Draw a bounding box around every parasitised red blood cell, every trophozoite, every gametocyte, every leukocyte, and every artifact (platelet-like body, stain precipitate, or debris).
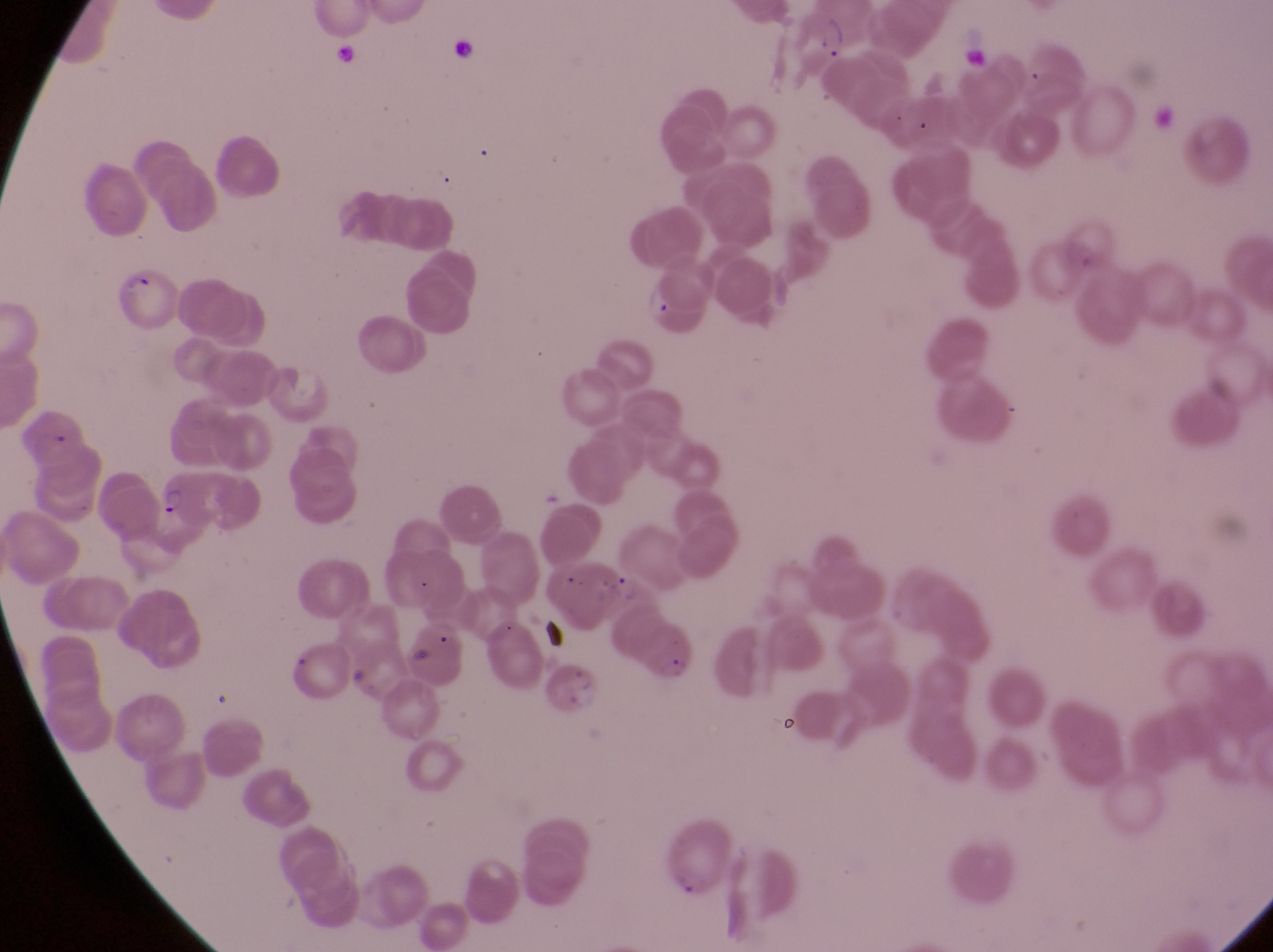
Approximate bounding boxes as left top right bottom in pixels.
Parasitised red blood cells: 118 267 181 337.
Trophozoites: 813 12 850 65; 642 277 672 322; 158 482 188 521; 611 564 648 612.
No leukocytes observed.
Artifacts (platelet-like body, stain precipitate, or debris): 447 30 486 72; 335 42 370 89; 535 616 574 658.

country: Uganda
capture: smartphone photograph through the eyepiece of an Olympus CX-23 microscope
magnification: 1000x
image_size: 1273×952 pixels
field_of_view: single
preparation: thin blood smear